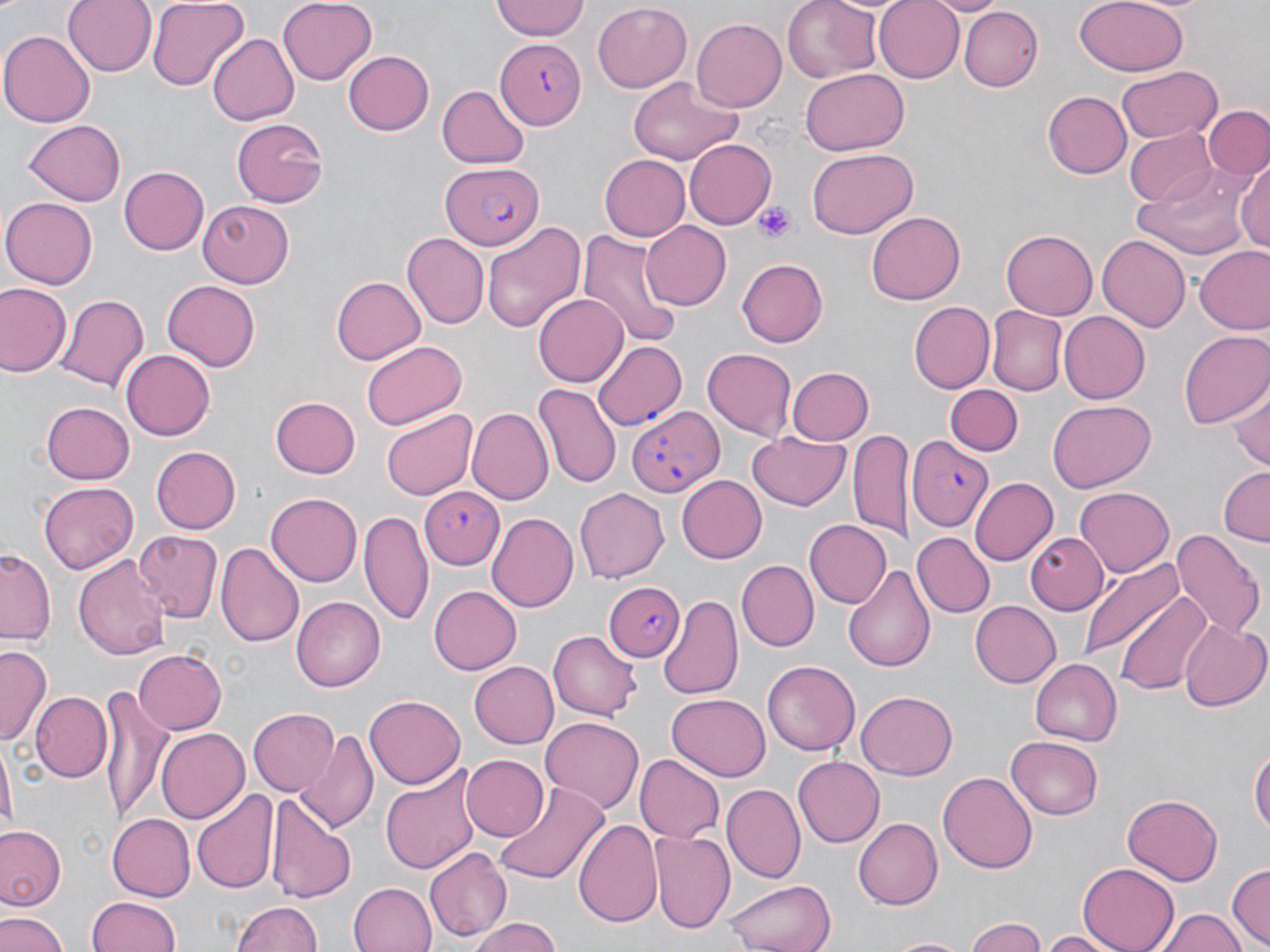

Summary:
  - Coordinate format: approximate bounding boxes as (x1,y1)-(x2,y2) corner pairs in pixels
  - Platelet locations: (753,201)-(799,241)
  - Uninfected red blood cell locations: (61,0)-(155,76), (147,0)-(247,90), (278,0)-(375,85), (488,0)-(591,42), (782,0)-(883,84), (870,0)-(965,83), (922,0)-(1007,16), (1075,0)-(1187,76), (593,1)-(693,90), (959,7)-(1043,91), (693,18)-(786,111), (0,31)-(95,125), (208,34)-(299,124), (343,49)-(433,134), (1114,67)-(1221,145), (800,70)-(906,155), (627,76)-(742,166), (438,85)-(527,169), (1041,89)-(1132,178), (1203,106)-(1269,182), (232,118)-(330,207), (25,119)-(126,205), (1124,128)-(1218,205), (685,138)-(779,229), (806,147)-(918,239), (598,154)-(690,242), (1236,157)-(1270,256), (1136,161)-(1255,259), (119,166)-(208,255), (2,195)-(97,288), (197,200)-(294,289), (867,212)-(965,305), (479,220)-(587,335), (641,220)-(732,310), (579,227)-(681,346), (1000,231)-(1097,320), (403,234)-(489,327), (1096,234)-(1192,331), (1194,246)-(1270,335), (737,258)-(830,349), (331,275)-(425,364), (163,281)-(261,371), (0,286)-(71,377), (55,294)-(148,395), (534,294)-(628,387), (907,300)-(994,393), (988,307)-(1066,394), (1057,311)-(1150,404), (1178,328)-(1270,429), (360,340)-(468,430), (121,347)-(214,438), (703,349)-(796,437), (786,366)-(874,446), (1229,381)-(1270,473), (535,383)-(620,489), (946,385)-(1021,456), (269,396)-(360,478), (42,399)-(134,481), (1048,400)-(1156,491), (469,406)-(551,503), (381,408)-(477,500), (851,427)-(913,547), (745,431)-(851,514), (151,446)-(241,534), (1216,466)-(1270,543), (675,475)-(767,564), (970,477)-(1057,563), (37,481)-(138,574), (1076,486)-(1175,577), (575,487)-(669,583), (264,490)-(360,584), (360,509)-(432,625), (487,512)-(578,614), (804,520)-(891,609), (1172,527)-(1264,642), (133,531)-(222,620), (913,532)-(994,617), (1027,532)-(1108,612), (217,542)-(303,649), (0,550)-(55,646), (74,552)-(170,659), (1079,554)-(1188,664), (737,561)-(818,651), (842,564)-(937,672), (427,585)-(521,674), (1114,589)-(1214,697), (659,594)-(742,697), (292,597)-(385,691), (968,599)-(1061,688), (1178,619)-(1269,712), (549,631)-(642,721), (0,646)-(50,747), (132,648)-(226,736), (1030,657)-(1122,745), (761,659)-(858,756), (469,661)-(560,749), (97,682)-(175,824), (29,690)-(113,783), (857,692)-(958,779), (668,693)-(770,779), (366,694)-(465,789), (248,708)-(338,797), (540,716)-(644,813), (155,728)-(248,824), (298,730)-(380,834), (1007,734)-(1103,818), (1,742)-(15,841), (1251,743)-(1270,845), (460,754)-(548,842), (635,754)-(723,843), (793,756)-(884,847), (380,764)-(482,875), (727,768)-(875,867), (939,772)-(1037,875), (725,784)-(802,882), (491,785)-(605,884), (192,790)-(279,894), (1121,793)-(1224,886), (269,795)-(354,903), (106,812)-(194,899), (852,817)-(943,910), (573,820)-(661,927), (0,823)-(66,911), (649,832)-(735,936), (424,848)-(512,942), (1079,862)-(1181,952), (1227,863)-(1270,948), (724,877)-(839,952), (347,881)-(438,952), (87,896)-(183,951), (231,900)-(322,952), (1152,908)-(1247,952), (0,911)-(69,952), (965,916)-(1051,952), (468,917)-(566,952), (1036,929)-(1124,952), (885,935)-(977,952)
  - Plasmodium falciparum-infected red blood cell locations: (496,38)-(586,131), (440,164)-(546,249), (592,340)-(687,428), (625,409)-(723,500), (908,438)-(990,531), (422,486)-(503,570), (604,581)-(684,663)
  - Slide-level diagnosis: Plasmodium falciparum
  - Preparation: thin blood film
  - Magnification: 1000x
  - Image size: 1270×952 pixels
  - Stain: May-Grünwald-Giemsa
  - Modality: optical microscopy
  - Field of view: one of a larger specimen